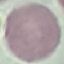

Result: no malaria parasites detected. Photographed with a smartphone camera at the microscope eyepiece. Automatically extracted cell patch, resized to 64 × 64 pixels. Giemsa stain. Thin blood film.